Assess the morphology of the red blood cells.
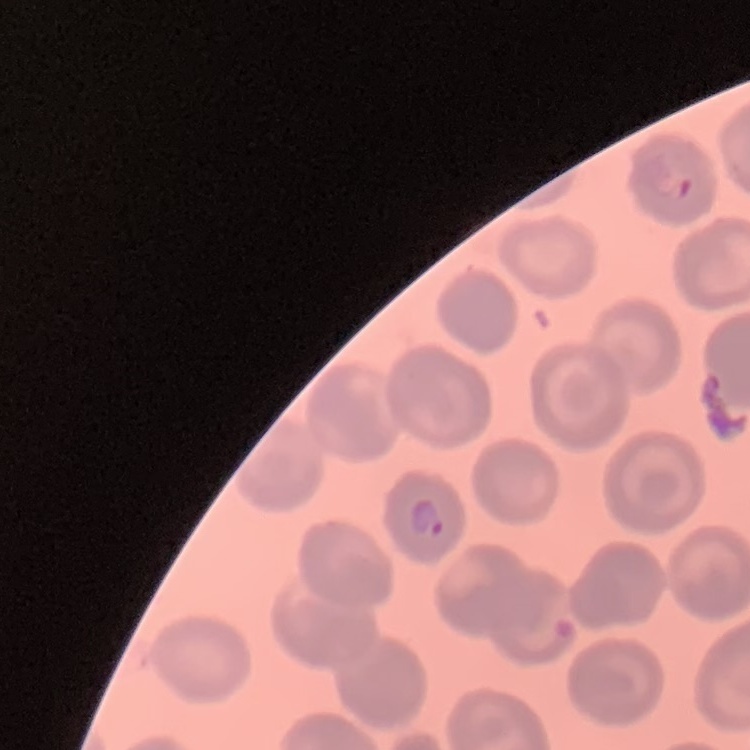
They show no rouleaux formation.

Thin peripheral smear. Square crop of a larger photomicrograph. Stained with either Field's or Giemsa.